Outline each Plasmodium malariae-infected red blood cell.
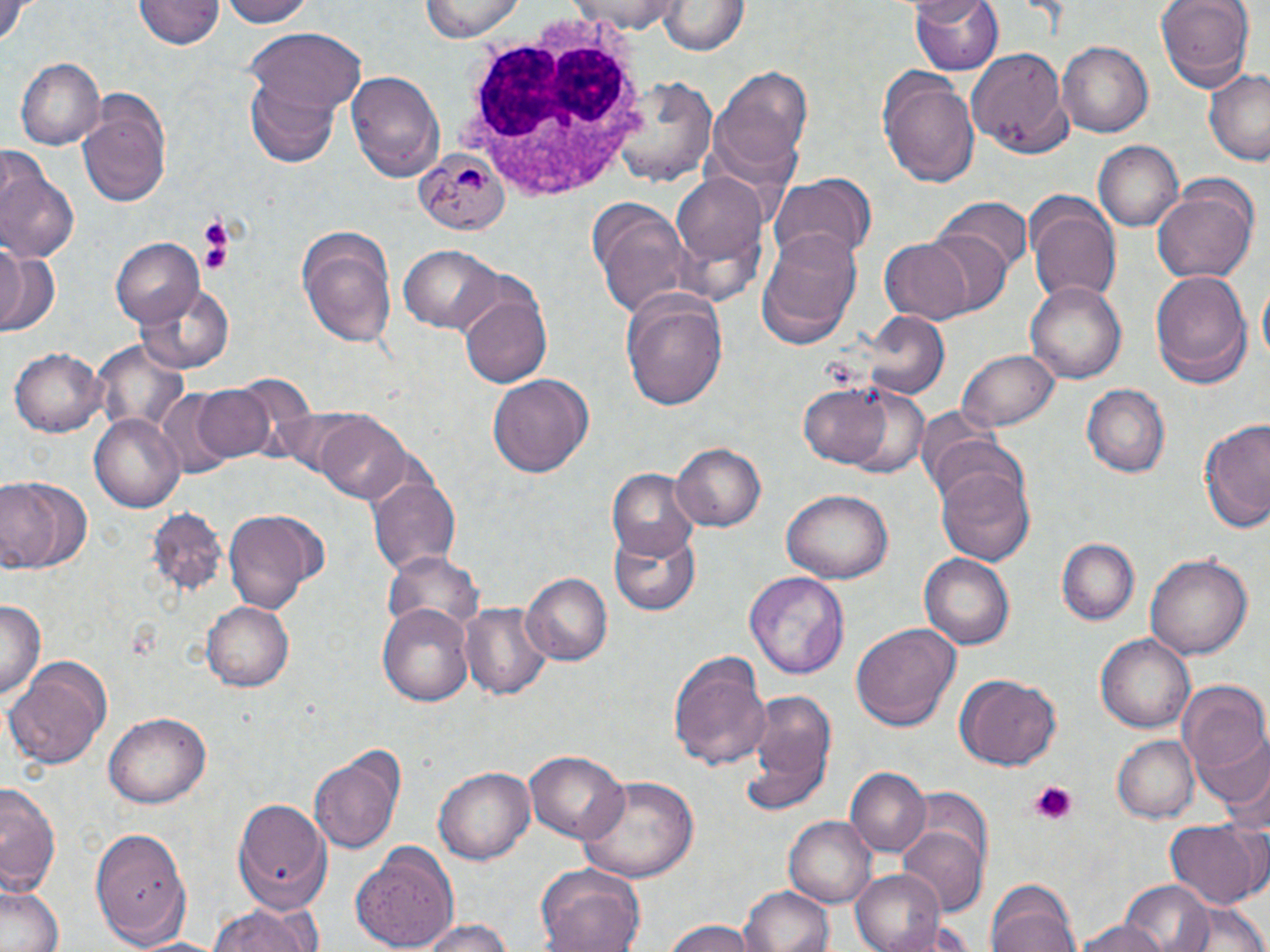
Approximate bounding boxes as (x1,y1)-(x2,y2) corner pairs in pixels.
Plasmodium malariae-infected red blood cells: (416,147)-(508,234).

Uninfected red blood cell locations: (220,0)-(313,27), (569,0)-(687,33), (910,0)-(1004,77), (1153,0)-(1258,92), (1,1)-(33,45), (136,1)-(222,52), (418,1)-(528,42), (659,2)-(748,55), (246,28)-(367,118), (1056,42)-(1152,138), (965,48)-(1072,157), (15,57)-(105,150), (715,66)-(814,169), (1202,68)-(1270,165), (879,69)-(980,188), (347,71)-(445,181), (611,73)-(717,185), (245,81)-(339,167), (78,102)-(170,211), (1091,140)-(1183,233), (0,165)-(80,267), (671,168)-(769,285), (767,174)-(874,269), (1152,179)-(1258,286), (934,196)-(1030,276), (1026,198)-(1121,306), (592,205)-(697,323), (296,225)-(399,351), (917,228)-(1011,319), (757,231)-(864,348), (110,238)-(205,328), (878,238)-(975,324), (0,244)-(56,336), (400,245)-(503,333), (1149,269)-(1250,386), (1023,278)-(1128,386), (135,281)-(238,376), (1257,281)-(1270,370), (460,290)-(554,389), (621,290)-(728,413), (863,314)-(949,403), (90,339)-(195,433), (9,346)-(107,436), (957,349)-(1059,434), (486,372)-(594,477), (799,381)-(895,468), (190,384)-(277,464), (840,385)-(934,478), (1082,385)-(1168,477), (310,411)-(412,501), (89,412)-(185,513), (1199,416)-(1270,534), (673,442)-(766,533), (935,461)-(1038,566), (609,469)-(700,562), (367,472)-(460,575), (0,477)-(90,577), (782,489)-(891,584), (144,507)-(228,599), (224,508)-(322,612), (612,531)-(700,616), (1058,538)-(1139,624), (387,550)-(485,641), (1145,551)-(1252,661), (920,554)-(1016,650), (744,570)-(850,679), (520,571)-(611,667), (0,597)-(44,703), (202,600)-(294,693), (456,600)-(551,702), (378,601)-(475,706), (850,621)-(959,731), (1094,633)-(1197,735), (670,652)-(772,770), (6,659)-(111,769), (955,674)-(1061,770), (1175,679)-(1270,775), (738,695)-(835,816), (102,712)-(209,809), (1193,723)-(1270,819), (1112,734)-(1197,823), (310,746)-(405,856), (522,748)-(628,843), (434,765)-(535,865), (848,768)-(928,856), (578,773)-(700,883), (0,780)-(62,899), (233,797)-(331,907), (785,816)-(877,909), (1166,819)-(1262,911), (87,823)-(193,943), (899,824)-(987,917), (350,846)-(459,952), (850,868)-(947,952), (537,869)-(645,952), (986,879)-(1081,952), (1118,880)-(1217,952), (0,882)-(65,952), (739,885)-(836,952), (205,900)-(319,952), (1172,901)-(1270,952), (418,918)-(517,952), (662,919)-(760,952), (1073,920)-(1175,952), (129,935)-(227,952). White blood cell locations: (458,19)-(651,207). Platelet locations: (202,224)-(233,276), (1028,782)-(1076,824). Slide-level diagnosis: Plasmodium malariae. Image is 1270×952 pixels. Optical microscopy. 1000x magnification. Thin blood smear. May-Grünwald-Giemsa-stained preparation. Single field of view.